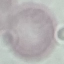
Malaria status: uninfected. Thin smear of blood. Cell patch, automatically extracted from a larger field of view and resized to 64 × 64 pixels. Giemsa stain. Photographed with a smartphone camera at the microscope eyepiece.